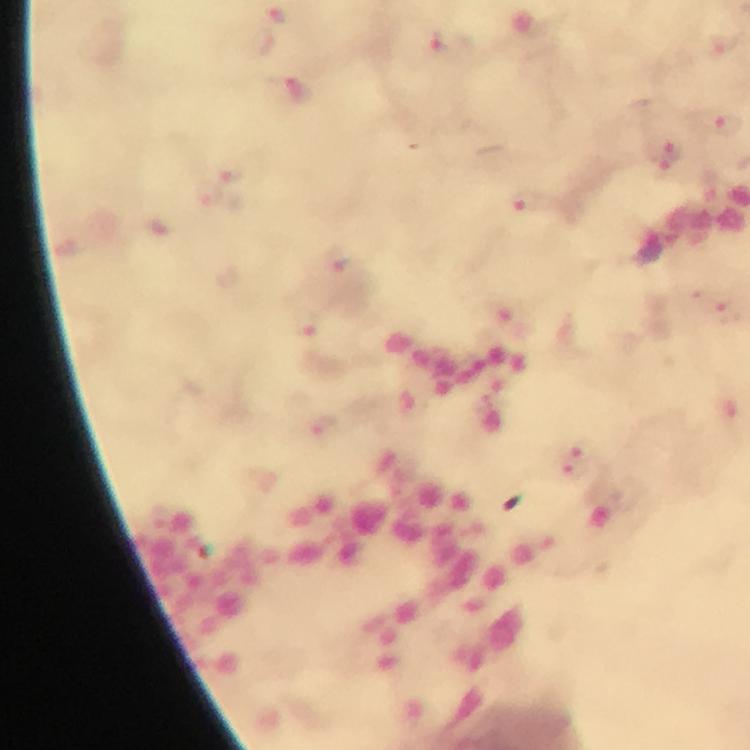 Approximate object centers, in pixels from the top-left corner. Malaria parasite locations: (x=276, y=16), (x=725, y=124), (x=670, y=149), (x=228, y=170), (x=667, y=171), (x=212, y=195), (x=526, y=200), (x=340, y=261), (x=728, y=311), (x=309, y=323), (x=323, y=424), (x=581, y=448), (x=574, y=466). Image is 750×750 pixels. Immersion oil was used. Giemsa stain. 100x magnification. From a diagnostic examination for malaria. A crop from one field of view. Photographed through the microscope with a smartphone camera. Thick smear.